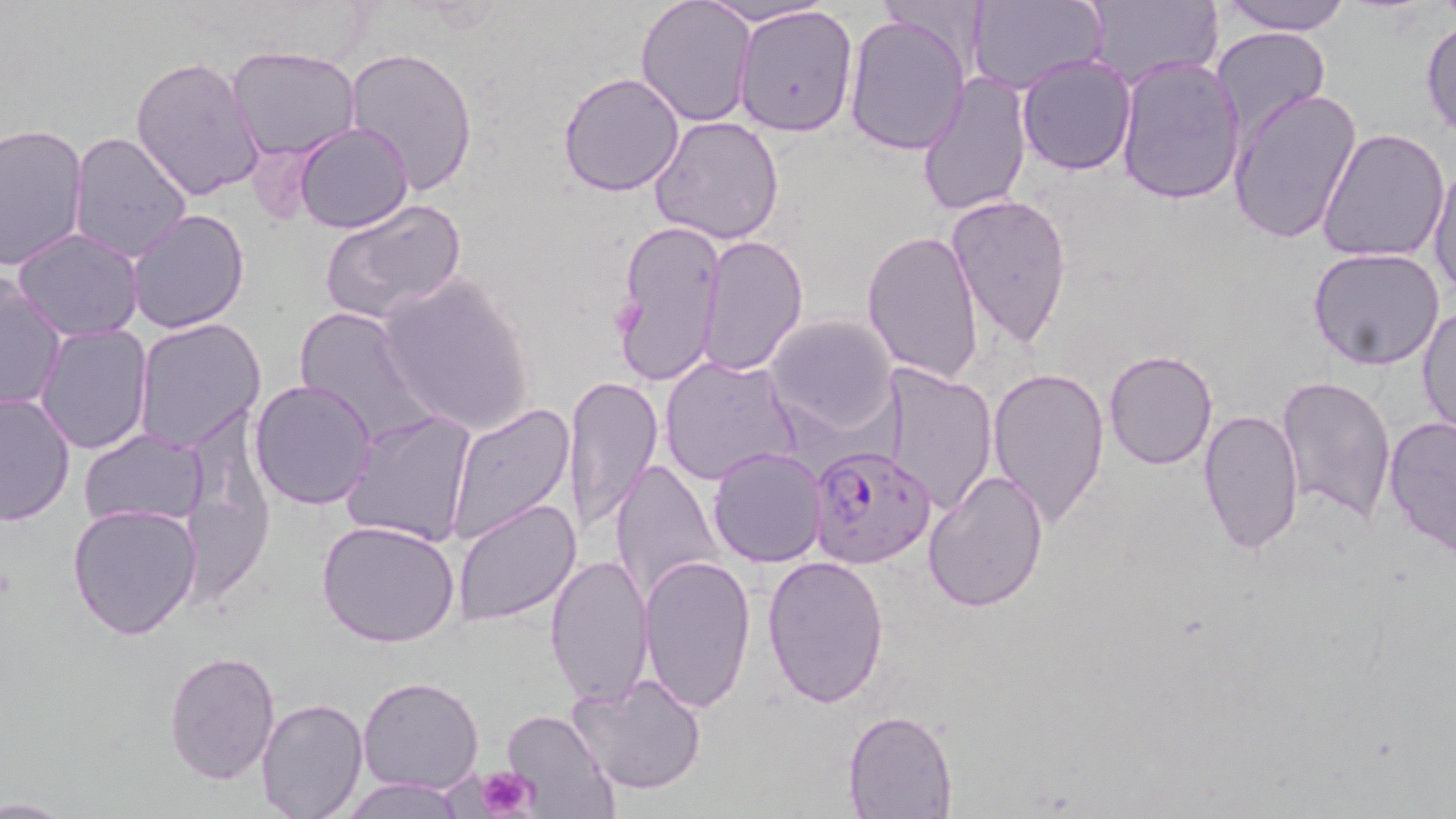

slide_level_diagnosis: Plasmodium falciparum
stain: May-Grünwald-Giemsa
preparation: thin blood smear
magnification: 1000x
image_size: 1456×819 pixels
modality: optical microscopy
field_of_view: single
uninfected_red_blood_cell_locations: 'approximate bounding boxes as named x1/y1/x2/y2 corners in pixels: (x1=698, y1=0, x2=839, y2=29), (x1=1084, y1=0, x2=1224, y2=91), (x1=1214, y1=0, x2=1353, y2=36), (x1=634, y1=1, x2=756, y2=127), (x1=967, y1=1, x2=1107, y2=93), (x1=733, y1=4, x2=859, y2=138), (x1=843, y1=13, x2=970, y2=157), (x1=1420, y1=15, x2=1456, y2=141), (x1=1209, y1=28, x2=1331, y2=142), (x1=226, y1=45, x2=362, y2=161), (x1=343, y1=48, x2=480, y2=195), (x1=1016, y1=51, x2=1137, y2=175), (x1=1113, y1=53, x2=1245, y2=204), (x1=130, y1=54, x2=266, y2=202), (x1=557, y1=70, x2=685, y2=197), (x1=916, y1=70, x2=1034, y2=218), (x1=1227, y1=86, x2=1362, y2=247), (x1=650, y1=114, x2=786, y2=246), (x1=0, y1=121, x2=90, y2=272), (x1=294, y1=122, x2=413, y2=234), (x1=1316, y1=127, x2=1450, y2=265), (x1=69, y1=131, x2=194, y2=264), (x1=1428, y1=156, x2=1456, y2=301), (x1=318, y1=194, x2=468, y2=327), (x1=946, y1=194, x2=1074, y2=350), (x1=127, y1=208, x2=253, y2=334), (x1=612, y1=217, x2=726, y2=389), (x1=11, y1=228, x2=145, y2=344), (x1=860, y1=229, x2=984, y2=386), (x1=700, y1=235, x2=808, y2=375), (x1=1307, y1=248, x2=1446, y2=370), (x1=0, y1=272, x2=66, y2=415), (x1=376, y1=273, x2=534, y2=436), (x1=1416, y1=304, x2=1456, y2=439), (x1=291, y1=305, x2=440, y2=449), (x1=765, y1=314, x2=898, y2=436), (x1=133, y1=317, x2=266, y2=454), (x1=35, y1=325, x2=155, y2=454), (x1=1102, y1=350, x2=1218, y2=471), (x1=659, y1=353, x2=800, y2=486), (x1=879, y1=364, x2=996, y2=516), (x1=989, y1=367, x2=1110, y2=528), (x1=563, y1=374, x2=665, y2=535), (x1=1278, y1=376, x2=1398, y2=526), (x1=249, y1=378, x2=377, y2=509), (x1=0, y1=389, x2=75, y2=525), (x1=446, y1=401, x2=576, y2=544), (x1=341, y1=408, x2=478, y2=548), (x1=1196, y1=408, x2=1303, y2=553), (x1=1383, y1=416, x2=1455, y2=560), (x1=80, y1=429, x2=207, y2=529), (x1=708, y1=446, x2=828, y2=567), (x1=609, y1=455, x2=724, y2=607), (x1=922, y1=470, x2=1050, y2=613), (x1=453, y1=498, x2=584, y2=627), (x1=66, y1=502, x2=202, y2=639), (x1=315, y1=519, x2=462, y2=648), (x1=638, y1=550, x2=757, y2=718), (x1=545, y1=552, x2=655, y2=707), (x1=762, y1=556, x2=891, y2=708), (x1=163, y1=650, x2=282, y2=785), (x1=570, y1=671, x2=708, y2=795), (x1=357, y1=677, x2=485, y2=795), (x1=255, y1=698, x2=369, y2=819), (x1=500, y1=709, x2=616, y2=816), (x1=843, y1=709, x2=958, y2=818), (x1=338, y1=778, x2=471, y2=818), (x1=0, y1=793, x2=71, y2=817)'
plasmodium_falciparum_infected_red_blood_cell_locations: 'approximate bounding boxes as named x1/y1/x2/y2 corners in pixels: (x1=808, y1=442, x2=937, y2=568)'
platelet_locations: 'approximate bounding boxes as named x1/y1/x2/y2 corners in pixels: (x1=476, y1=766, x2=540, y2=819)'